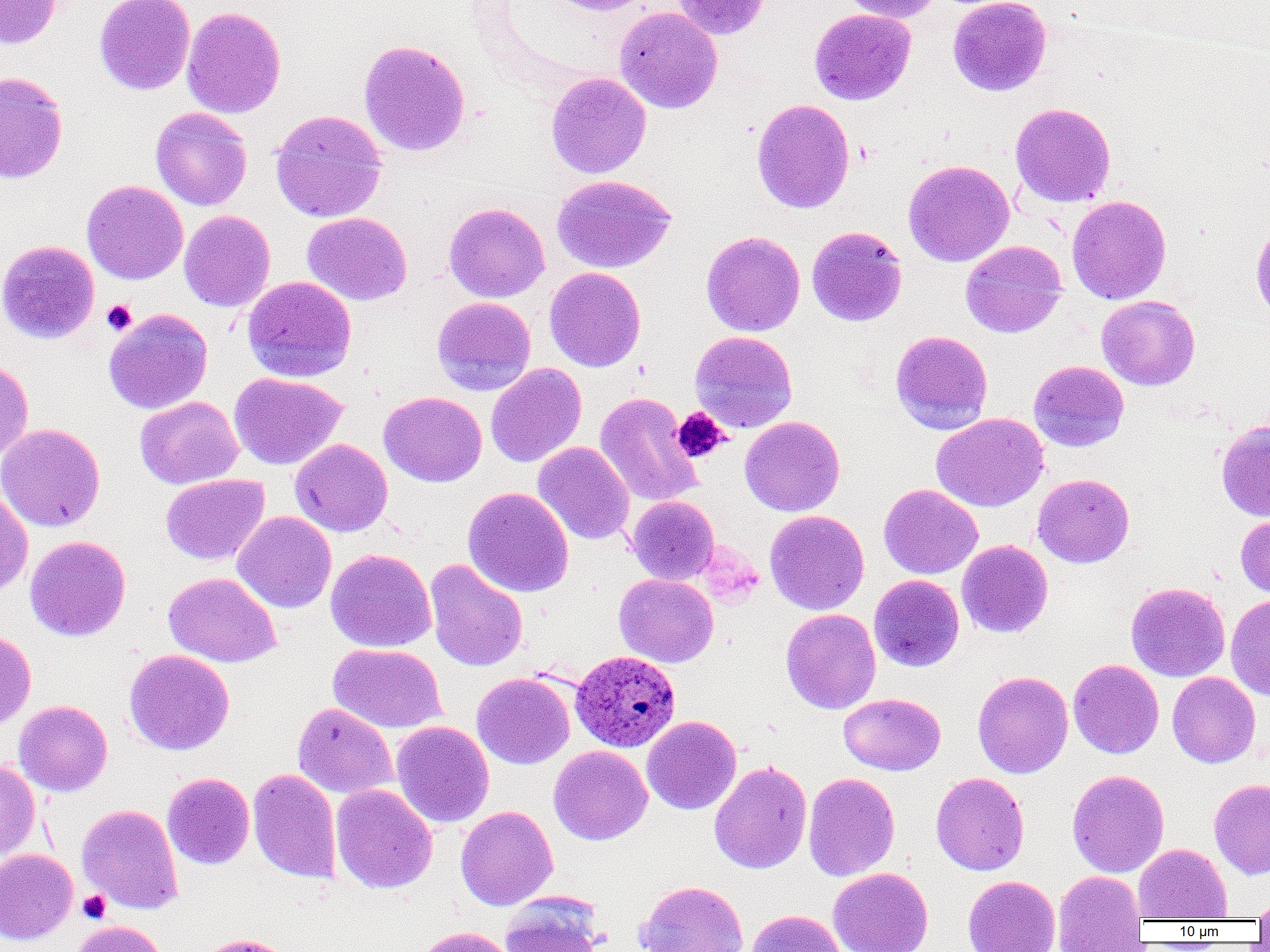

Summary:
  - Coordinate format: approximate bounding boxes as [x1, y1, x2, y2] in pixels
  - Uninfected red blood cell locations (subset): [0, 0, 61, 49], [94, 0, 195, 95], [547, 0, 655, 16], [671, 0, 772, 39], [837, 0, 941, 22], [948, 0, 1051, 96], [181, 6, 286, 119], [615, 7, 723, 114], [809, 8, 916, 105], [359, 39, 471, 157], [0, 72, 69, 183], [546, 72, 651, 179], [751, 98, 855, 213], [1010, 102, 1116, 208], [150, 107, 252, 211], [270, 109, 387, 222], [903, 159, 1015, 267], [551, 174, 676, 273], [82, 179, 188, 284], [1067, 195, 1171, 305], [443, 203, 549, 303], [179, 210, 276, 312], [302, 212, 412, 305], [1251, 222, 1270, 324], [807, 226, 907, 327], [701, 231, 805, 336], [0, 240, 100, 344], [960, 240, 1067, 338], [544, 266, 646, 372], [242, 276, 357, 382], [1097, 295, 1200, 390], [431, 296, 536, 396], [103, 308, 213, 414], [890, 330, 993, 434], [690, 331, 798, 433], [0, 359, 33, 462], [1028, 360, 1129, 452], [485, 363, 587, 467], [229, 372, 348, 470], [379, 391, 487, 487], [595, 392, 702, 507], [135, 396, 243, 489], [931, 413, 1048, 512], [740, 415, 845, 516], [1216, 419, 1270, 522], [0, 423, 105, 532], [290, 438, 393, 537], [532, 441, 634, 545], [161, 474, 270, 565], [1033, 474, 1134, 567], [878, 484, 983, 579], [463, 487, 574, 597], [0, 488, 33, 595], [627, 496, 719, 585], [765, 510, 870, 615], [232, 511, 336, 613], [1235, 513, 1270, 600], [25, 535, 131, 642], [957, 539, 1053, 638], [326, 548, 436, 652], [426, 559, 528, 672], [163, 572, 280, 667], [614, 573, 718, 667], [869, 574, 964, 672], [1126, 582, 1230, 682], [1226, 594, 1270, 700], [781, 608, 881, 714], [0, 629, 36, 730], [328, 643, 447, 733], [123, 649, 235, 755], [1068, 659, 1164, 758], [972, 670, 1073, 778], [1167, 671, 1260, 768], [471, 672, 575, 769], [839, 693, 945, 775], [13, 700, 113, 796], [292, 702, 398, 800], [642, 716, 742, 815], [391, 721, 494, 828], [549, 745, 652, 845], [0, 759, 41, 862], [709, 760, 812, 874], [248, 768, 342, 883], [1067, 769, 1169, 878], [163, 772, 254, 869], [803, 772, 900, 881], [931, 772, 1029, 875], [1209, 778, 1270, 879], [331, 784, 437, 894], [77, 804, 183, 914], [456, 805, 558, 910], [1133, 843, 1232, 921], [0, 849, 78, 944], [828, 867, 934, 952], [1053, 870, 1146, 950], [963, 875, 1060, 952], [635, 880, 749, 952], [1251, 895, 1270, 923], [499, 896, 603, 952], [746, 909, 847, 952], [70, 920, 169, 952], [412, 926, 516, 952], [196, 933, 297, 952]
  - Platelet locations (subset): [101, 299, 137, 336], [671, 407, 730, 464], [78, 890, 111, 923]
  - Plasmodium ovale-infected red blood cell locations: [570, 650, 681, 752]
  - Slide-level diagnosis: Plasmodium ovale
  - Preparation: thin blood film
  - Field of view: single
  - Magnification: 1000x
  - Modality: optical microscopy
  - Image size: 1270×952 pixels